Assess for malaria.
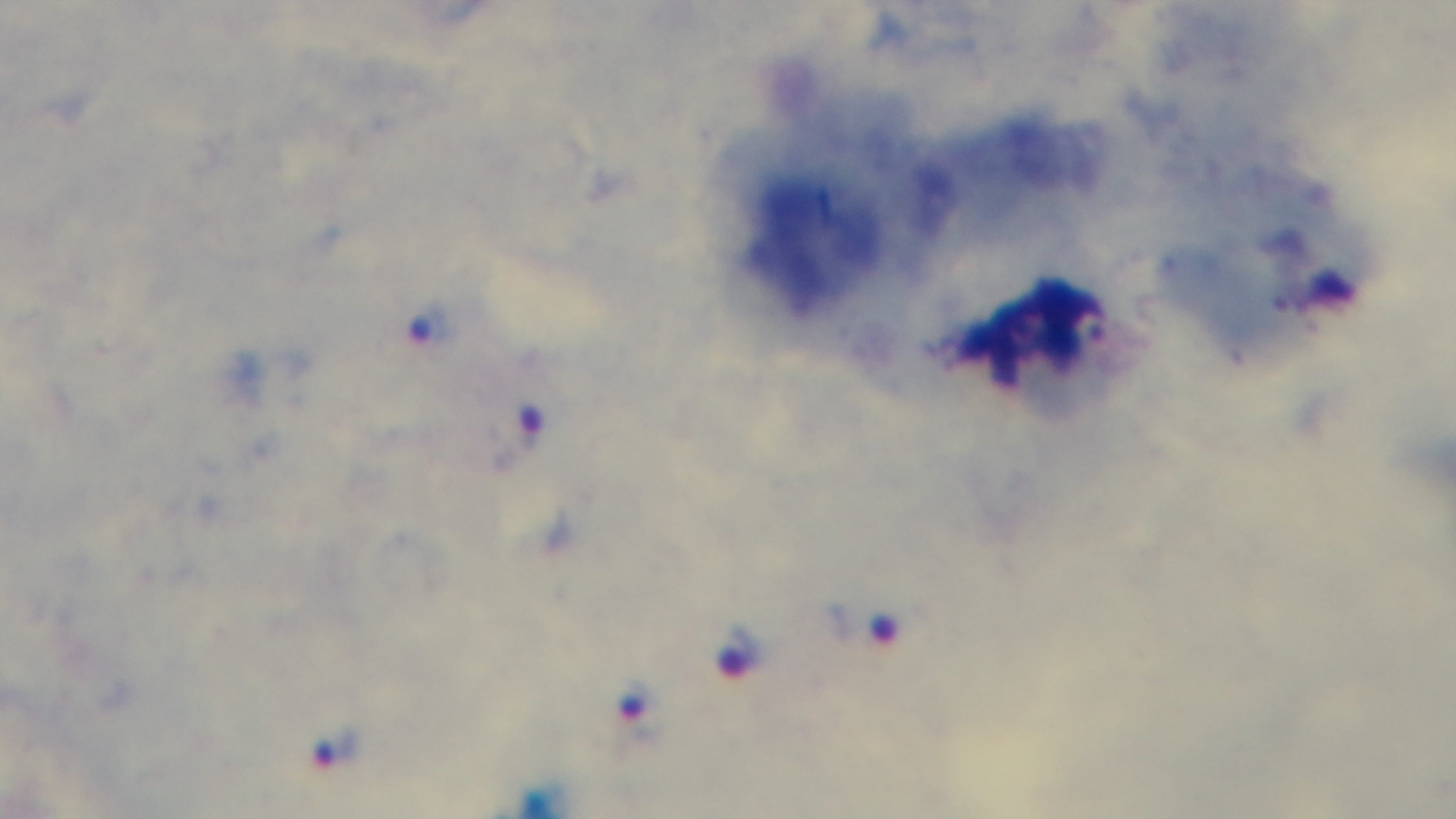

Positive.

capture: mounted 4K digital camera
preparation: thick smear
stain: Giemsa
field_of_view: single
objective: 100x oil immersion
modality: light microscopy